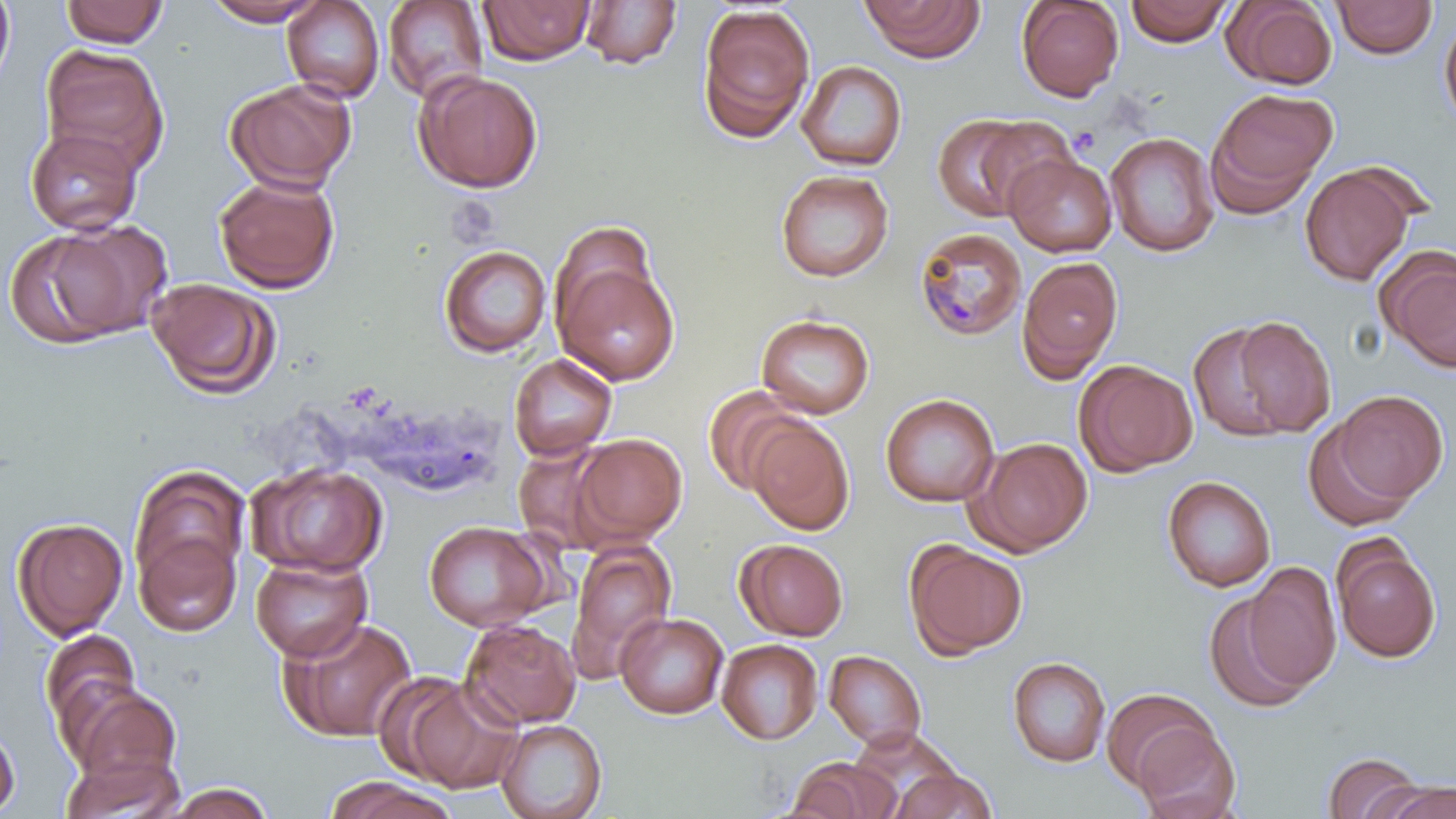

slide-level diagnosis = Plasmodium malariae
uninfected red blood cell locations = approximate bounding boxes as (x1,y1)-(x2,y2) corner pairs in pixels: (0,0)-(16,94), (202,0)-(327,26), (859,0)-(985,62), (1016,0)-(1124,102), (1223,0)-(1337,89), (1331,0)-(1438,60), (60,1)-(169,48), (282,1)-(385,103), (382,1)-(489,103), (479,1)-(596,65), (578,1)-(683,69), (1124,1)-(1234,46), (696,4)-(815,144), (1439,14)-(1456,132), (265,31)-(380,164), (41,44)-(170,178), (797,60)-(908,171), (414,70)-(543,193), (225,79)-(356,193), (1206,88)-(1337,214), (931,114)-(1048,222), (25,126)-(143,235), (1105,132)-(1220,257), (1004,152)-(1117,257), (1300,163)-(1416,287), (775,169)-(894,282), (213,174)-(340,293), (12,220)-(169,348), (550,221)-(658,336), (439,244)-(551,357), (440,247)-(675,367), (1378,247)-(1456,372), (553,256)-(680,386), (1016,256)-(1124,382), (147,277)-(281,399), (756,313)-(875,419), (1228,313)-(1337,437), (1186,320)-(1300,443), (508,352)-(617,461), (1074,359)-(1197,477), (702,385)-(805,496), (1328,390)-(1448,505), (880,393)-(999,507), (1302,415)-(1419,533), (746,417)-(855,536), (571,433)-(687,545), (968,437)-(1093,556), (246,461)-(388,576), (128,464)-(251,595), (1162,475)-(1277,593), (12,517)-(128,640), (422,520)-(553,632), (133,526)-(242,637), (1331,536)-(1441,663), (736,539)-(849,641), (566,540)-(677,681), (905,540)-(1028,661), (251,554)-(372,662), (1242,561)-(1342,692), (1205,589)-(1312,713), (615,612)-(728,719), (278,616)-(418,743), (460,620)-(581,729), (39,629)-(143,735), (717,639)-(823,745), (823,650)-(927,751), (1007,657)-(1111,768), (395,674)-(524,794), (64,682)-(182,789), (1102,688)-(1217,793), (496,719)-(607,819), (0,720)-(20,816), (1132,721)-(1241,819), (851,728)-(965,810), (60,751)-(185,819), (1322,751)-(1425,819), (787,758)-(899,818), (890,768)-(997,818), (325,776)-(460,818), (1379,780)-(1456,819), (163,782)-(276,819)
magnification = 1000x
Plasmodium malariae-infected red blood cell locations = approximate bounding boxes as (x1,y1)-(x2,y2) corner pairs in pixels: (913,227)-(1027,342)
image size = 1456×819 pixels
field of view = single
preparation = thin blood smear
modality = optical microscopy
stain = May-Grünwald-Giemsa